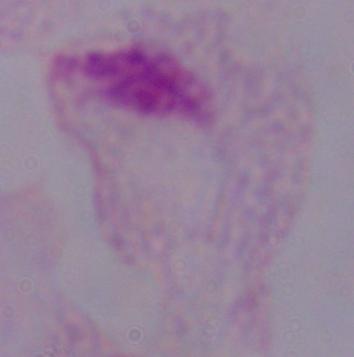

magnification = 1000x
identification = trichomonad
modality = photomicrograph